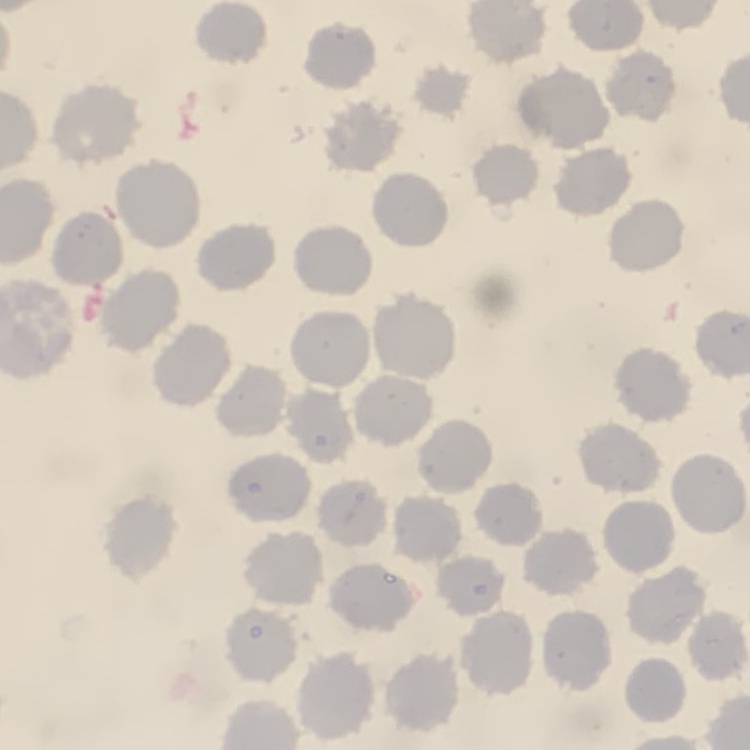

The red blood cells exhibit no rouleaux formation. Thin peripheral smear. Stained with either Field's or Giemsa. Square crop of a larger photomicrograph.